Assess the morphology of the red blood cells.
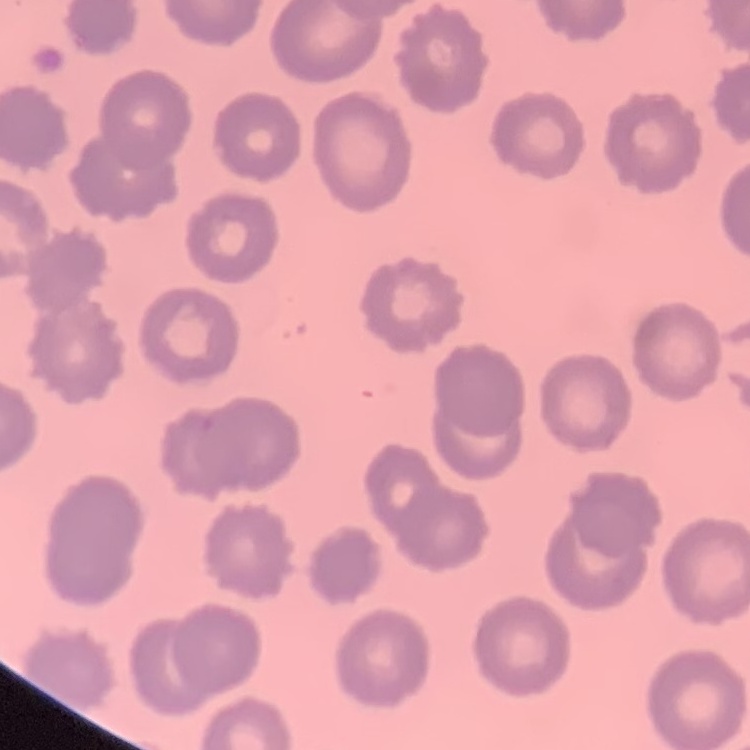
No rouleaux formation.

One tile cut from a larger photomicrograph. Thin blood smear. Field's or Giemsa stain.